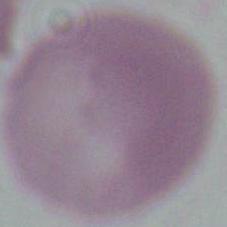
modality = micrograph
identification = red blood cell
magnification = 1000x